Report the malaria status of this cell.
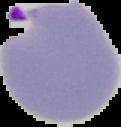
Parasitized.

Summary:
  - Image type: segmented cell region with the area outside set to black
  - Preparation: thin blood smear
  - Image size: 121×127 pixels